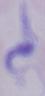

1000x magnification. Photomicrograph. A trypanosome is shown.